State which parasite is depicted.
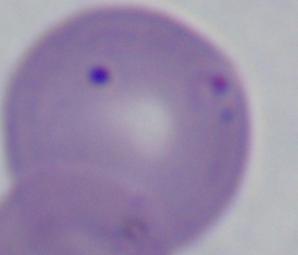

This is Babesia.

{
  "magnification": "1000x",
  "modality": "photomicrograph"
}